Locate every blood parasite and identify its species.
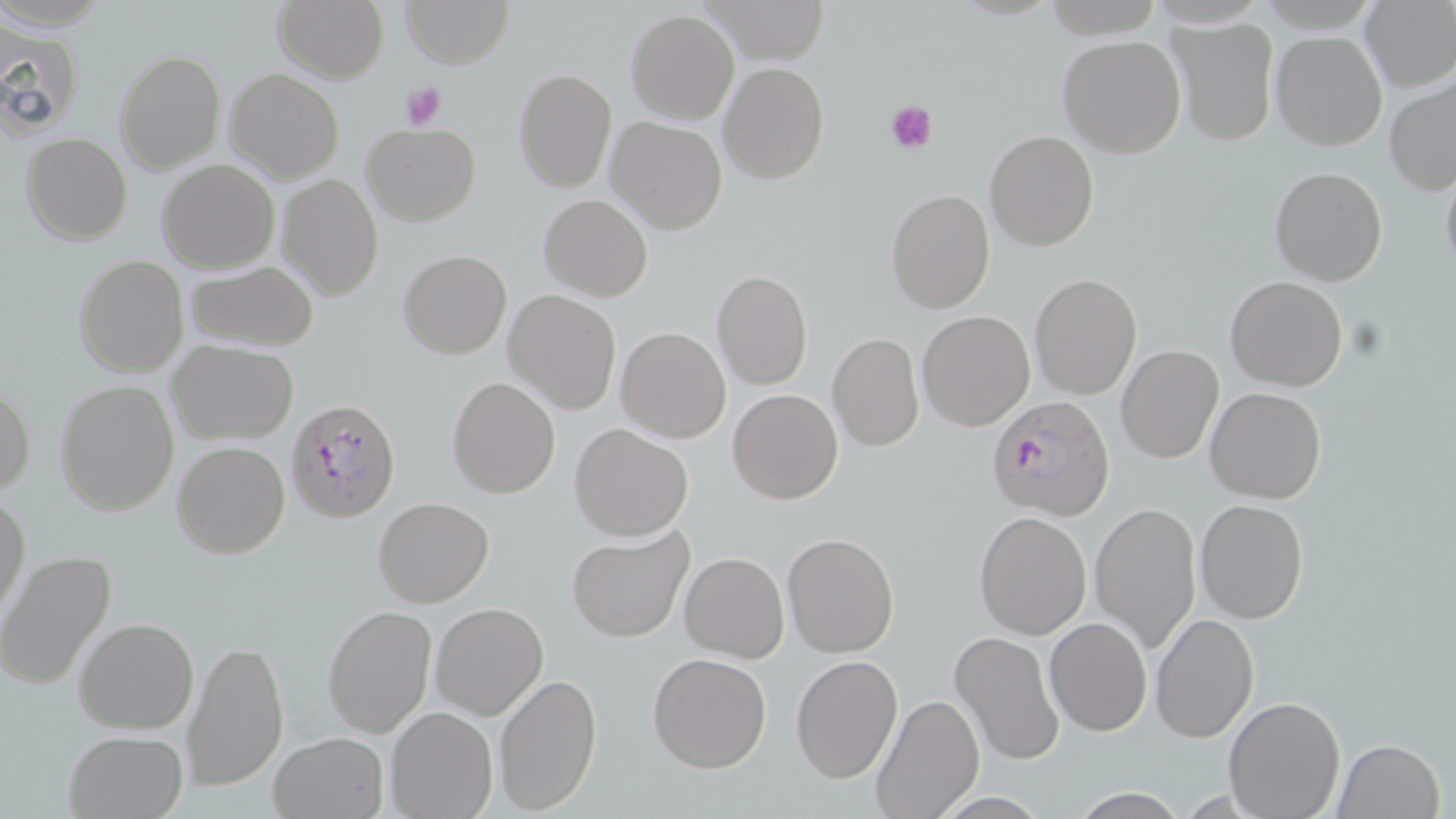

Approximate bounding boxes as named x1/y1/x2/y2 corners in pixels.
Plasmodium falciparum-infected red blood cells: (x1=985, y1=393, x2=1117, y2=521), (x1=284, y1=396, x2=399, y2=523).
No Plasmodium ovale, Plasmodium malariae, Plasmodium vivax, Babesia divergens, or Trypanosoma brucei observed.

slide-level diagnosis = Plasmodium falciparum
magnification = 1000x
platelet locations = approximate bounding boxes as named x1/y1/x2/y2 corners in pixels: (x1=398, y1=80, x2=447, y2=131), (x1=884, y1=97, x2=939, y2=154)
modality = light microscopy
stain = May-Grünwald-Giemsa
field of view = one of a larger specimen
preparation = thin blood film
image size = 1456×819 pixels
uninfected red blood cell locations = approximate bounding boxes as named x1/y1/x2/y2 corners in pixels: (x1=274, y1=0, x2=388, y2=84), (x1=401, y1=0, x2=513, y2=68), (x1=700, y1=0, x2=828, y2=65), (x1=1357, y1=0, x2=1456, y2=92), (x1=626, y1=9, x2=741, y2=124), (x1=1168, y1=16, x2=1280, y2=146), (x1=0, y1=25, x2=85, y2=140), (x1=1271, y1=30, x2=1388, y2=151), (x1=1058, y1=35, x2=1186, y2=157), (x1=114, y1=49, x2=225, y2=174), (x1=719, y1=62, x2=828, y2=184), (x1=225, y1=68, x2=344, y2=183), (x1=513, y1=68, x2=619, y2=193), (x1=1384, y1=73, x2=1456, y2=198), (x1=605, y1=116, x2=728, y2=236), (x1=362, y1=124, x2=481, y2=226), (x1=984, y1=129, x2=1099, y2=251), (x1=21, y1=132, x2=132, y2=244), (x1=157, y1=159, x2=280, y2=274), (x1=1440, y1=163, x2=1456, y2=279), (x1=1269, y1=166, x2=1387, y2=285), (x1=278, y1=173, x2=383, y2=302), (x1=885, y1=189, x2=995, y2=313), (x1=538, y1=193, x2=653, y2=302), (x1=398, y1=250, x2=511, y2=359), (x1=73, y1=255, x2=189, y2=378), (x1=183, y1=260, x2=320, y2=352), (x1=710, y1=270, x2=813, y2=391), (x1=1030, y1=272, x2=1142, y2=399), (x1=1225, y1=275, x2=1348, y2=390), (x1=503, y1=290, x2=622, y2=415), (x1=918, y1=310, x2=1035, y2=431), (x1=615, y1=327, x2=732, y2=443), (x1=827, y1=332, x2=924, y2=452), (x1=168, y1=341, x2=299, y2=445), (x1=1116, y1=344, x2=1224, y2=463), (x1=447, y1=375, x2=561, y2=499), (x1=0, y1=379, x2=36, y2=496), (x1=55, y1=381, x2=180, y2=516), (x1=1206, y1=386, x2=1327, y2=503), (x1=728, y1=389, x2=843, y2=503), (x1=569, y1=422, x2=693, y2=542), (x1=172, y1=441, x2=290, y2=558), (x1=0, y1=488, x2=29, y2=619), (x1=371, y1=497, x2=494, y2=607), (x1=1195, y1=499, x2=1309, y2=623), (x1=1089, y1=501, x2=1202, y2=653), (x1=973, y1=512, x2=1092, y2=639), (x1=566, y1=527, x2=692, y2=642), (x1=781, y1=532, x2=899, y2=658), (x1=0, y1=550, x2=120, y2=691), (x1=680, y1=552, x2=788, y2=663), (x1=428, y1=603, x2=548, y2=721), (x1=322, y1=604, x2=437, y2=740), (x1=1151, y1=611, x2=1259, y2=744), (x1=74, y1=618, x2=200, y2=735), (x1=1046, y1=618, x2=1152, y2=736), (x1=949, y1=629, x2=1066, y2=767), (x1=182, y1=637, x2=289, y2=793), (x1=647, y1=652, x2=773, y2=773), (x1=790, y1=654, x2=902, y2=782), (x1=492, y1=671, x2=603, y2=816), (x1=871, y1=693, x2=985, y2=819), (x1=1224, y1=696, x2=1345, y2=818), (x1=387, y1=707, x2=498, y2=819), (x1=63, y1=729, x2=188, y2=818), (x1=269, y1=730, x2=388, y2=818), (x1=1333, y1=739, x2=1446, y2=819), (x1=1066, y1=787, x2=1191, y2=818)